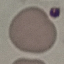

Summary:
  - Result: negative for malaria parasites
  - Preparation: thin blood smear
  - Capture: smartphone through the microscope eyepiece
  - Stain: Giemsa
  - Image type: cell patch, automatically extracted from a larger field of view and resized to 64 × 64 pixels